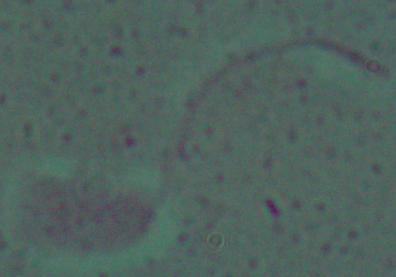
magnification = 1000x
modality = photomicrograph
identification = Leishmania